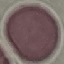

Malaria status: uninfected. Giemsa-stained preparation. Acquired by smartphone through the microscope eyepiece. Thin blood smear. Automatically extracted cell patch, resized to 64 × 64 pixels.